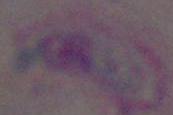
Summary:
  - Modality: photomicrograph
  - Identification: Toxoplasma gondii
  - Magnification: 1000x